Identify the preparation type.
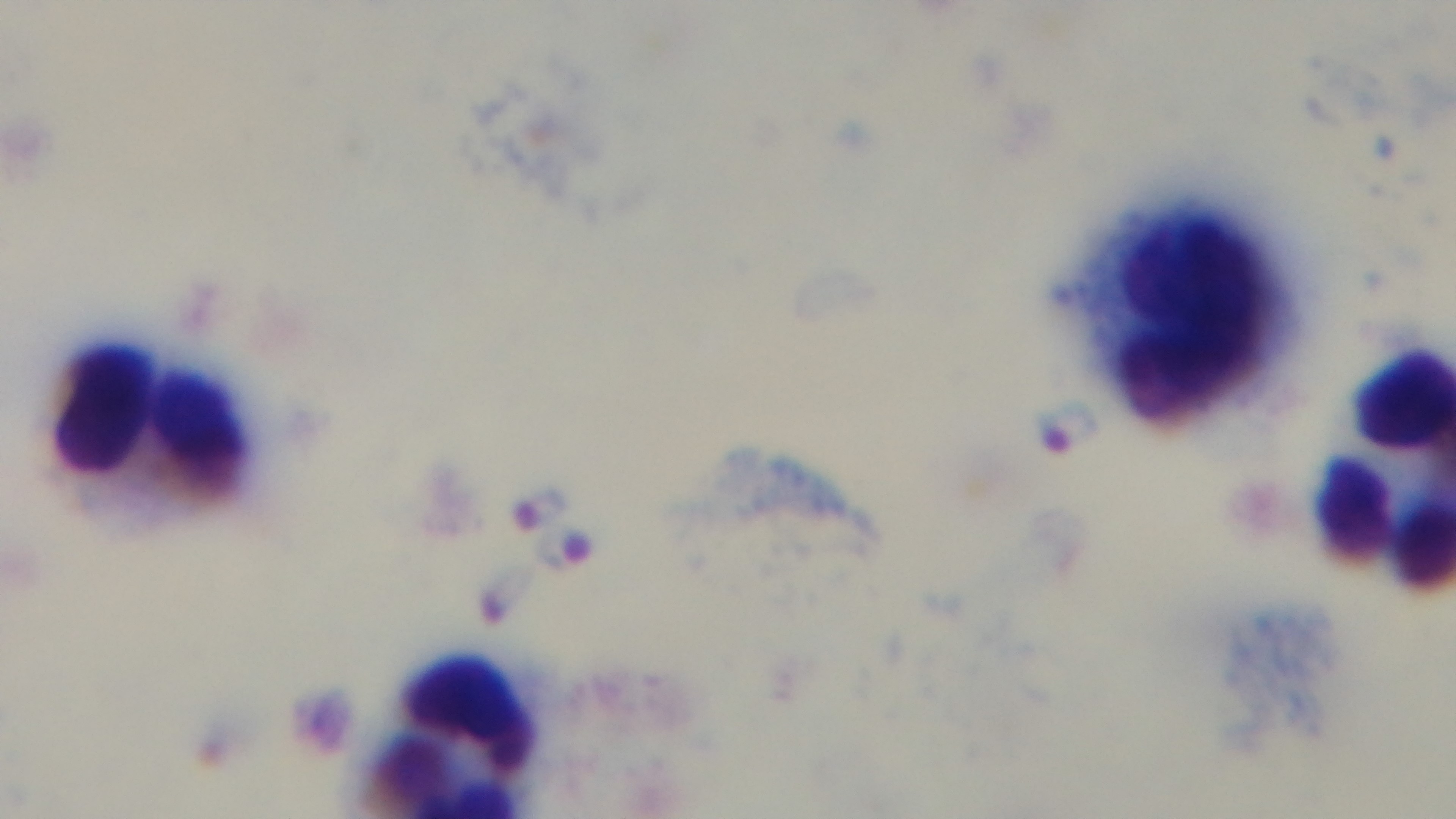

It is a thick blood film.

Single field of view. 100x oil-immersion objective. Malaria status: positive. Giemsa-stained. Light microscopy. Captured with a mounted 4K digital camera.